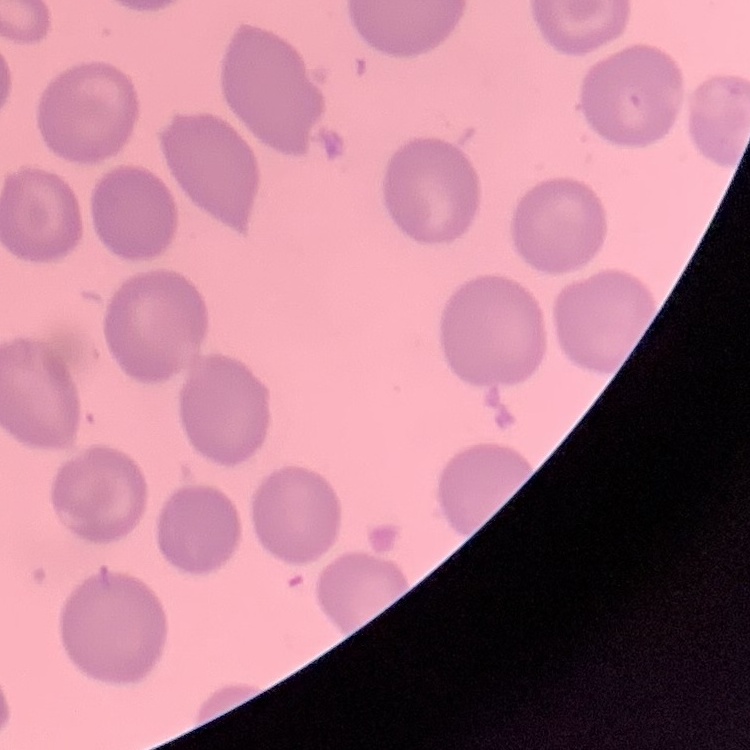

Summary:
  - Erythrocyte morphology: no rouleaux formation
  - Image type: one tile cut from a larger photomicrograph
  - Preparation: thin peripheral smear
  - Stain: Field's or Giemsa